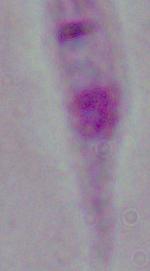 A Leishmania parasite is seen. Photomicrograph. 1000x magnification.